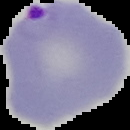

Malaria status: parasitized. Image is 130×130 pixels. From a thin blood film. The area outside the segmented cell region is set to black.